Find each cell and give its type.
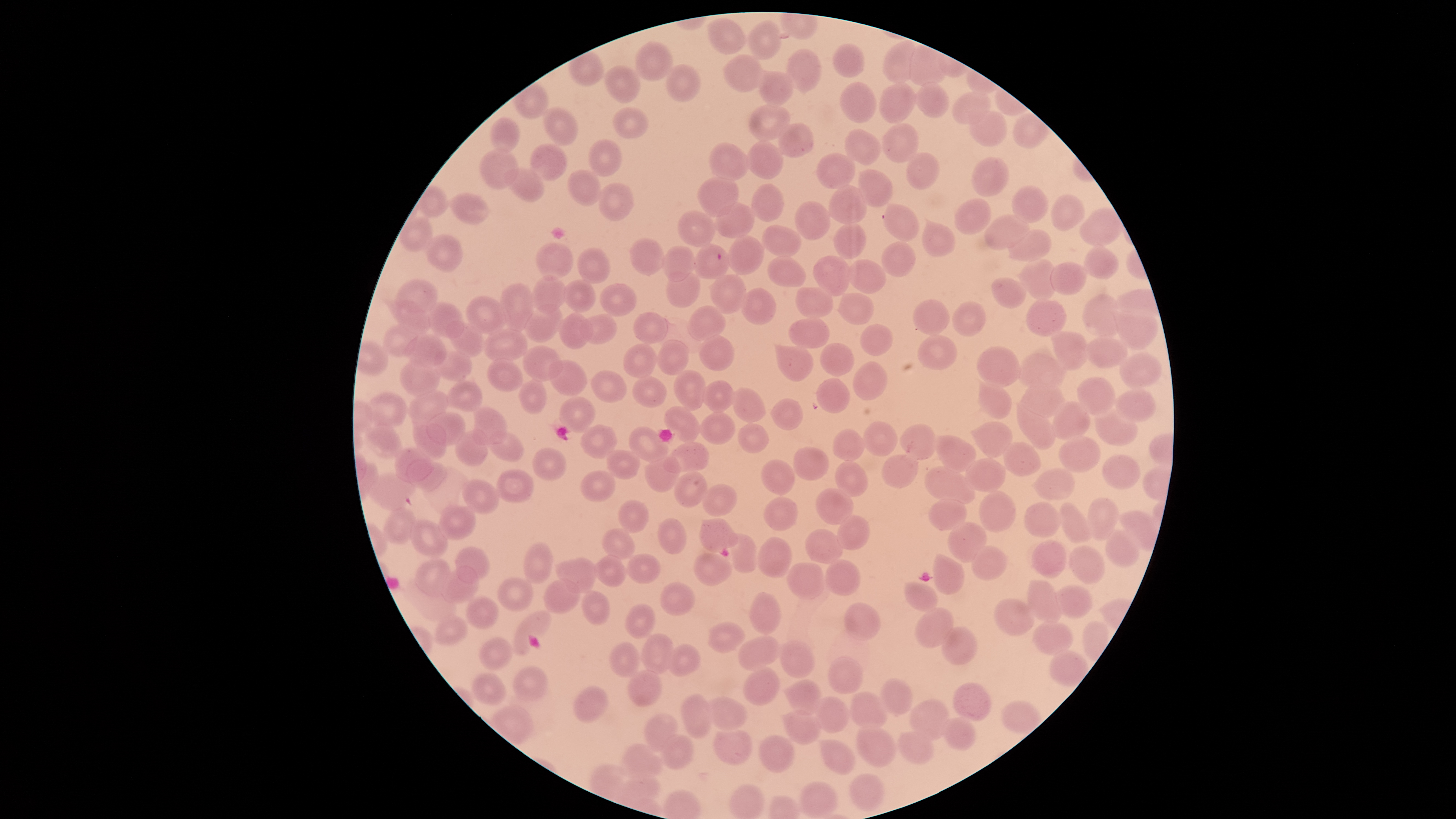
Approximate bounding boxes as {left, top, right, bottom} in pixels.
Parasitized red blood cells: {694, 244, 729, 279}.
Uninfected red blood cells: {707, 17, 746, 54}, {748, 21, 781, 60}, {882, 40, 920, 82}, {635, 42, 673, 81}, {834, 44, 865, 77}, {787, 49, 822, 92}, {724, 54, 764, 92}, {665, 64, 701, 102}, {605, 65, 641, 103}, {757, 71, 793, 107}, {839, 82, 877, 123}, {914, 82, 949, 119}, {878, 83, 916, 123}, {952, 91, 990, 125}, {750, 104, 791, 142}, {543, 107, 579, 146}, {612, 107, 648, 137}, {969, 111, 1007, 147}, {491, 116, 521, 153}, {778, 123, 814, 159}, {882, 123, 919, 163}, {844, 128, 882, 166}, {590, 139, 623, 177}, {747, 141, 783, 180}, {708, 142, 751, 181}, {531, 144, 568, 182}, {480, 147, 520, 190}, {816, 152, 855, 189}, {907, 152, 939, 189}, {971, 158, 1010, 197}, {504, 168, 544, 201}, {858, 169, 894, 207}, {568, 170, 602, 206}, {698, 177, 739, 218}, {598, 182, 634, 221}, {751, 184, 784, 222}, {829, 184, 866, 224}, {1012, 186, 1048, 223}, {450, 193, 489, 225}, {1051, 194, 1084, 231}, {955, 198, 991, 236}, {795, 201, 830, 240}, {715, 203, 755, 238}, {884, 204, 918, 242}, {677, 210, 717, 247}, {985, 215, 1029, 250}, {922, 221, 955, 256}, {834, 222, 867, 259}, {763, 225, 801, 257}, {1006, 229, 1051, 262}, {425, 235, 462, 273}, {727, 236, 764, 275}, {629, 238, 665, 275}, {537, 241, 573, 280}, {882, 241, 915, 276}, {663, 246, 695, 283}, {1085, 246, 1119, 279}, {578, 247, 611, 284}, {813, 256, 851, 297}, {767, 257, 806, 287}, {1020, 259, 1058, 300}, {847, 260, 887, 294}, {1050, 263, 1087, 295}, {666, 272, 700, 307}, {530, 275, 568, 313}, {710, 275, 746, 314}, {992, 278, 1027, 309}, {395, 279, 438, 312}, {564, 280, 594, 313}, {502, 283, 534, 331}, {599, 284, 637, 317}, {795, 286, 834, 319}, {740, 288, 776, 326}, {838, 293, 874, 325}, {1082, 294, 1122, 339}, {466, 296, 508, 335}, {913, 299, 949, 335}, {392, 300, 431, 334}, {1026, 301, 1067, 337}, {426, 302, 464, 338}, {952, 302, 986, 336}, {524, 304, 563, 343}, {687, 306, 727, 340}, {559, 312, 593, 349}, {632, 312, 668, 344}, {1116, 312, 1157, 351}, {580, 314, 618, 344}, {788, 317, 830, 349}, {446, 321, 484, 357}, {860, 324, 894, 356}, {383, 325, 418, 358}, {482, 329, 529, 362}, {1054, 332, 1091, 370}, {403, 334, 447, 366}, {700, 335, 735, 372}, {917, 335, 958, 371}, {1084, 336, 1128, 369}, {659, 340, 689, 376}, {623, 343, 658, 379}, {820, 343, 855, 376}, {522, 345, 564, 382}, {776, 346, 813, 382}, {976, 346, 1022, 386}, {434, 350, 472, 381}, {1119, 352, 1161, 388}, {1018, 353, 1067, 390}, {399, 358, 441, 398}, {486, 359, 524, 391}, {549, 360, 588, 396}, {853, 361, 888, 400}, {673, 369, 706, 410}, {590, 370, 627, 402}, {632, 376, 668, 408}, {816, 377, 851, 412}, {1077, 377, 1116, 416}, {519, 379, 546, 414}, {702, 380, 735, 413}, {446, 381, 484, 411}, {978, 381, 1012, 420}, {1021, 383, 1066, 418}, {732, 388, 766, 423}, {407, 390, 449, 425}, {1115, 390, 1156, 423}, {366, 391, 407, 426}, {559, 397, 595, 433}, {771, 398, 802, 430}, {1051, 401, 1091, 440}, {1016, 403, 1057, 450}, {665, 406, 701, 442}, {473, 407, 507, 445}, {1094, 407, 1138, 446}, {425, 413, 466, 444}, {701, 413, 735, 444}, {412, 419, 447, 460}, {863, 420, 898, 457}, {973, 421, 1013, 459}, {364, 423, 402, 458}, {738, 423, 769, 453}, {899, 424, 938, 460}, {580, 425, 618, 459}, {629, 427, 670, 462}, {833, 429, 865, 461}, {455, 430, 489, 465}, {488, 431, 525, 461}, {936, 434, 977, 473}, {1059, 436, 1101, 473}, {664, 442, 709, 473}, {1003, 442, 1041, 476}, {394, 447, 432, 482}, {531, 447, 568, 479}, {793, 447, 829, 480}, {606, 449, 641, 479}, {882, 454, 918, 489}, {1103, 454, 1140, 490}, {645, 455, 681, 492}, {406, 458, 447, 491}, {965, 458, 1006, 493}, {760, 459, 794, 496}, {835, 460, 868, 497}, {925, 466, 975, 505}, {1035, 467, 1075, 501}, {497, 469, 534, 502}, {580, 471, 615, 501}, {675, 471, 708, 507}, {368, 473, 415, 509}, {460, 479, 500, 514}, {700, 483, 737, 517}, {816, 488, 855, 527}, {979, 490, 1016, 533}, {1086, 496, 1119, 542}, {762, 497, 799, 532}, {929, 499, 967, 531}, {618, 500, 649, 533}, {1024, 502, 1062, 538}, {438, 504, 477, 540}, {1058, 504, 1093, 544}, {383, 507, 415, 544}, {836, 514, 870, 551}, {657, 517, 687, 554}, {700, 518, 739, 552}, {410, 519, 448, 558}, {947, 522, 987, 563}, {602, 528, 635, 560}, {805, 528, 844, 563}, {1105, 529, 1140, 568}, {730, 533, 757, 573}, {758, 536, 792, 578}, {1032, 539, 1067, 579}, {525, 541, 551, 583}, {971, 545, 1008, 580}, {1070, 545, 1105, 584}, {456, 546, 490, 585}, {933, 551, 964, 595}, {692, 552, 733, 586}, {592, 554, 626, 587}, {626, 554, 662, 583}, {415, 558, 451, 598}, {557, 558, 596, 594}, {824, 559, 861, 595}, {786, 563, 824, 600}, {441, 566, 478, 604}, {497, 577, 533, 612}, {543, 578, 582, 614}, {905, 582, 937, 613}, {1026, 582, 1064, 624}, {661, 583, 695, 616}, {1056, 586, 1092, 619}, {581, 591, 610, 627}, {749, 593, 781, 635}, {466, 594, 498, 631}, {994, 598, 1036, 636}, {626, 603, 655, 638}, {844, 603, 881, 639}, {914, 608, 955, 648}, {514, 611, 551, 655}, {436, 615, 469, 647}, {1032, 621, 1074, 656}, {707, 622, 745, 652}, {941, 626, 978, 665}, {642, 634, 673, 675}, {480, 636, 512, 671}, {738, 637, 779, 671}, {609, 641, 640, 678}, {777, 642, 816, 680}, {666, 644, 700, 677}, {1049, 650, 1089, 687}, {828, 657, 864, 694}, {513, 667, 548, 703}, {743, 667, 780, 706}, {628, 669, 662, 708}, {472, 674, 506, 705}, {881, 678, 914, 715}, {786, 680, 822, 714}, {954, 682, 992, 722}, {572, 684, 607, 723}, {679, 692, 712, 740}, {851, 692, 888, 729}, {702, 696, 748, 731}, {815, 697, 851, 734}, {910, 700, 949, 741}, {1000, 701, 1041, 734}, {783, 709, 821, 746}, {643, 714, 679, 751}, {943, 719, 977, 752}, {858, 724, 896, 769}, {713, 726, 753, 765}, {897, 732, 934, 764}, {661, 734, 695, 770}, {758, 734, 796, 773}, {819, 740, 855, 775}, {619, 744, 663, 781}, {849, 775, 885, 812}, {799, 782, 839, 819}.
No white blood cells identified.

Smartphone photograph through the microscope eyepiece. Thin smear of blood. The visible region is circular. Image is 1456×819 pixels. One field of view of the specimen. Species: Plasmodium falciparum. Giemsa-stained preparation.